Identify the parasite.
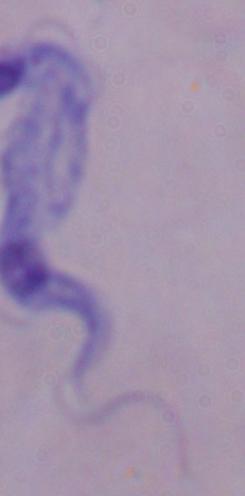

A trypanosome.

modality = photomicrograph
magnification = 1000x